Classify this cell by malaria status.
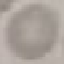

It is uninfected.

Thin blood film. Giemsa-stained preparation. Automatically extracted cell patch, resized to 64 × 64 pixels. Acquired by smartphone through the microscope eyepiece.